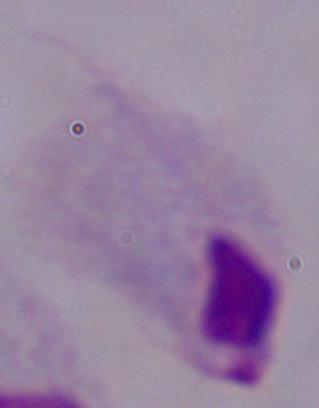

A trichomonad is seen. Micrograph. 1000x magnification.